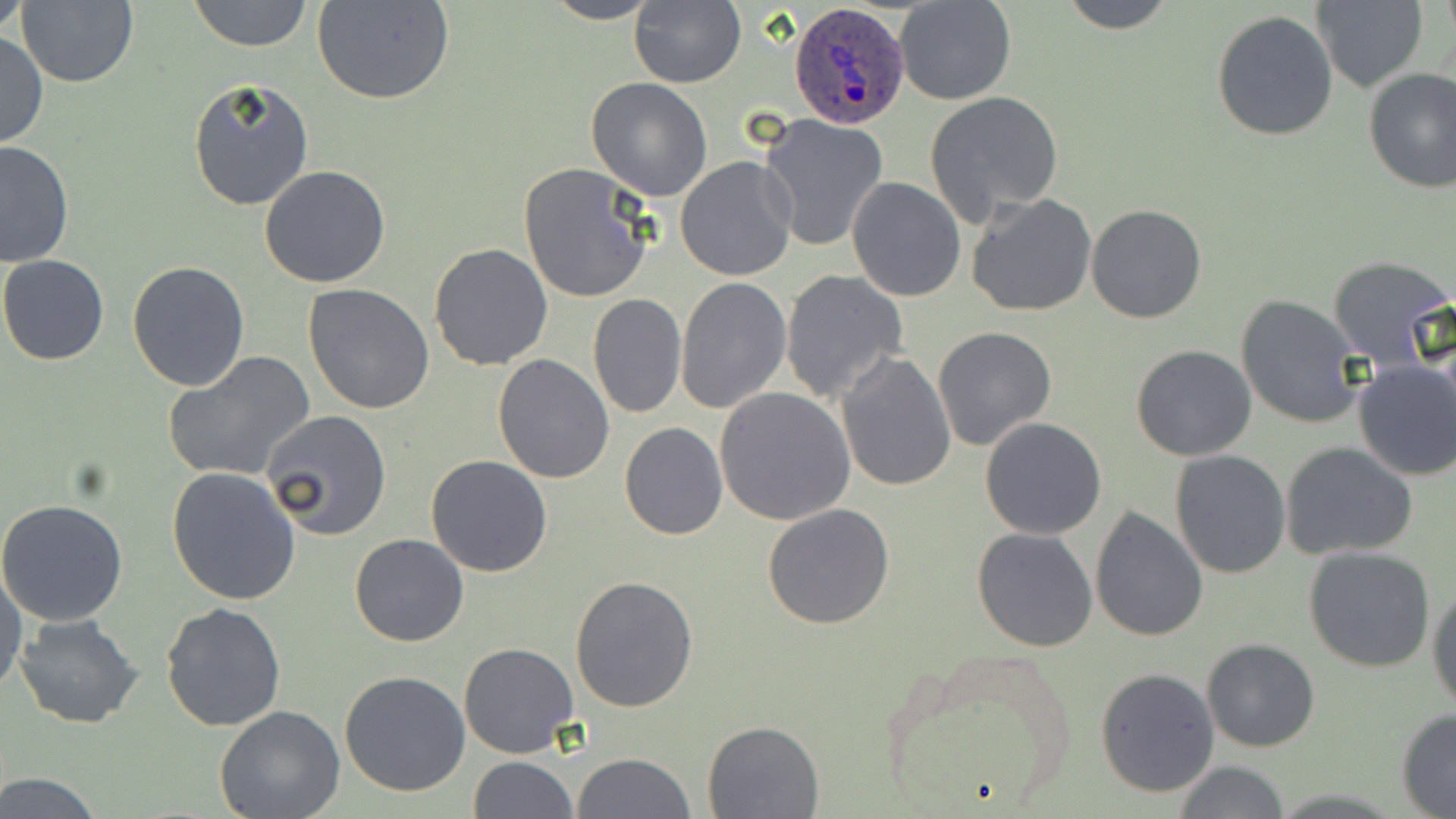
slide-level diagnosis = Plasmodium ovale
field of view = single
modality = light microscopy
uninfected red blood cell locations = approximate bounding boxes as (x1, y1, x2, y2) in pixels: (1, 0, 33, 37), (188, 0, 313, 51), (540, 0, 663, 24), (628, 0, 746, 88), (895, 0, 1016, 104), (1055, 0, 1181, 32), (1310, 0, 1429, 92), (16, 1, 138, 88), (314, 1, 455, 105), (1211, 9, 1339, 142), (0, 32, 47, 150), (1363, 67, 1456, 192), (186, 75, 314, 213), (586, 78, 713, 200), (925, 91, 1063, 224), (758, 112, 889, 253), (0, 141, 74, 268), (676, 157, 797, 281), (518, 163, 657, 304), (258, 165, 390, 287), (845, 176, 965, 302), (965, 194, 1097, 317), (1086, 205, 1206, 323), (428, 242, 555, 371), (0, 255, 109, 365), (1328, 255, 1455, 372), (128, 261, 250, 390), (780, 269, 909, 403), (677, 276, 791, 415), (303, 283, 436, 415), (586, 293, 687, 419), (1235, 295, 1366, 430), (933, 325, 1057, 451), (1130, 343, 1257, 460), (835, 350, 958, 493), (163, 352, 316, 482), (493, 354, 616, 483), (1351, 360, 1456, 482), (716, 387, 858, 525), (260, 410, 391, 540), (979, 417, 1107, 540), (619, 422, 728, 540), (1280, 442, 1418, 560), (1170, 450, 1291, 578), (425, 455, 553, 576), (167, 468, 302, 605), (0, 498, 129, 626), (762, 503, 896, 630), (1089, 507, 1209, 643), (971, 528, 1096, 651), (349, 532, 470, 646), (1304, 547, 1437, 673), (0, 563, 24, 700), (570, 574, 699, 712), (1429, 584, 1456, 711), (160, 603, 286, 732), (14, 614, 146, 728), (1201, 638, 1321, 752), (870, 640, 1081, 817), (459, 641, 578, 757), (1095, 667, 1221, 798), (339, 670, 471, 796), (214, 707, 345, 819), (1396, 707, 1456, 815), (701, 720, 825, 818), (572, 751, 694, 819), (468, 756, 578, 818), (1172, 761, 1292, 818), (0, 773, 109, 817)
image size = 1456×819 pixels
Plasmodium ovale-infected red blood cell locations = approximate bounding boxes as (x1, y1, x2, y2) in pixels: (790, 3, 912, 128)
magnification = 1000x
stain = May-Grünwald-Giemsa
preparation = thin blood film